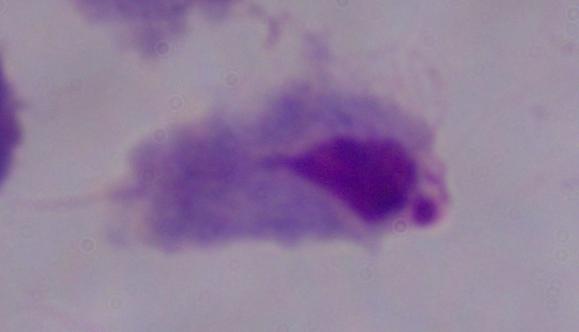
Summary:
  - Identification: trichomonad
  - Modality: micrograph
  - Magnification: 1000x